Locate and identify every blood parasite.
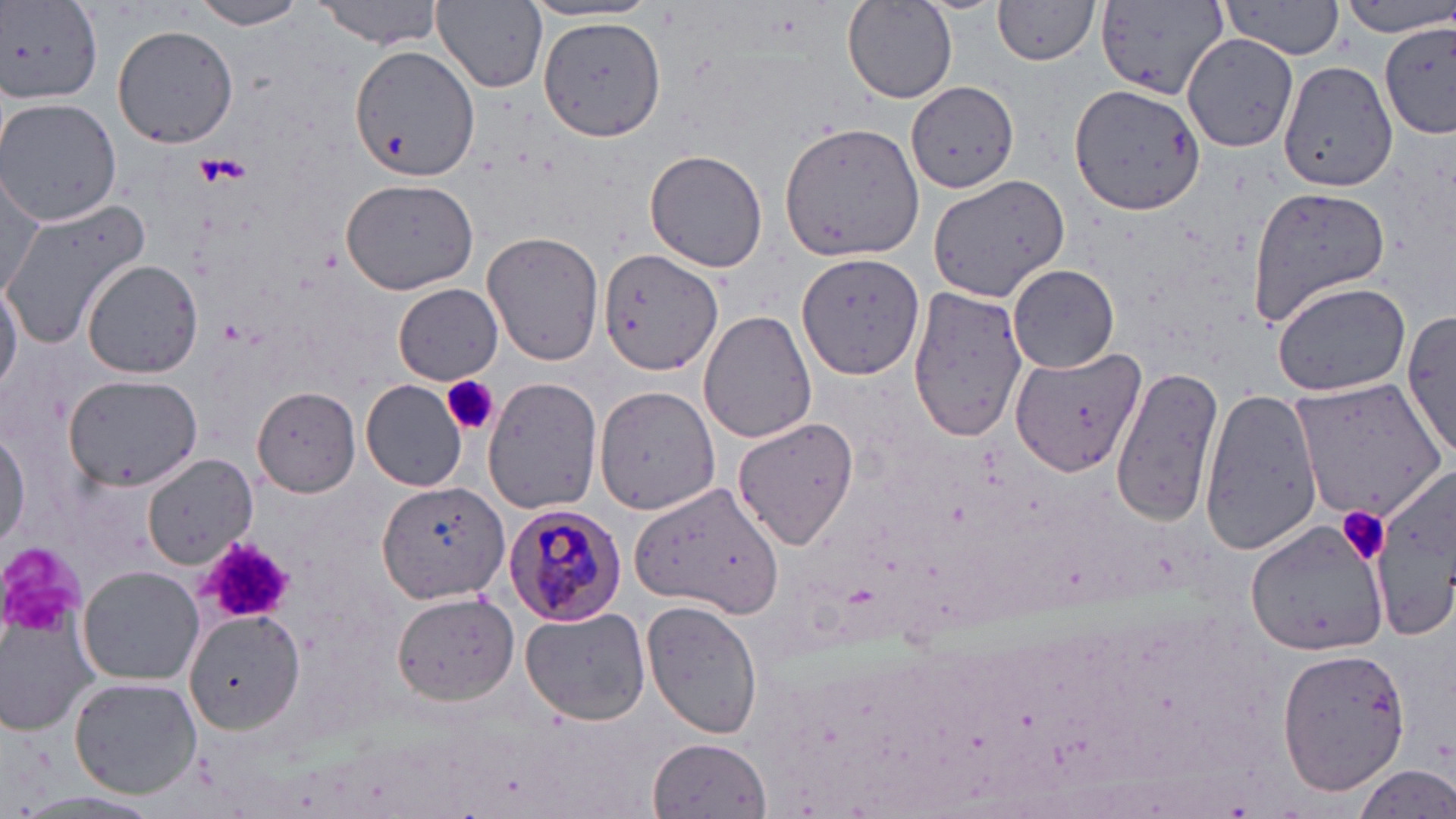
Approximate bounding boxes as (x1, y1, x2, y2) in pixels.
Plasmodium malariae-infected red blood cells: (502, 505, 627, 626).
No Plasmodium falciparum, Plasmodium ovale, Plasmodium vivax, Babesia divergens, or Trypanosoma brucei observed.

Summary:
  - Uninfected red blood cell locations: (314, 0, 447, 48), (433, 0, 548, 90), (1336, 0, 1456, 38), (189, 1, 308, 30), (992, 1, 1103, 65), (3, 2, 102, 103), (843, 2, 957, 102), (1218, 2, 1347, 57), (520, 3, 662, 26), (1091, 3, 1227, 104), (540, 15, 667, 141), (1378, 22, 1456, 137), (112, 25, 238, 150), (1183, 33, 1302, 153), (351, 45, 481, 182), (1279, 59, 1399, 192), (907, 81, 1019, 195), (1068, 81, 1208, 216), (0, 98, 122, 226), (779, 120, 925, 262), (644, 150, 769, 273), (2, 175, 48, 301), (927, 175, 1069, 299), (340, 176, 481, 295), (1246, 185, 1390, 319), (1, 200, 150, 347), (483, 232, 605, 368), (600, 246, 723, 376), (797, 253, 925, 380), (82, 260, 203, 380), (1009, 264, 1119, 373), (0, 273, 23, 398), (1270, 279, 1411, 397), (393, 283, 504, 384), (909, 287, 1026, 442), (698, 311, 816, 444), (1404, 312, 1456, 456), (1009, 335, 1139, 480), (1110, 361, 1227, 530), (64, 374, 200, 491), (483, 378, 602, 516), (1292, 378, 1450, 520), (362, 380, 468, 490), (594, 384, 723, 516), (252, 387, 361, 496), (1200, 387, 1321, 555), (733, 416, 859, 549), (0, 433, 26, 549), (142, 453, 258, 569), (1370, 473, 1455, 641), (628, 480, 785, 617), (378, 481, 511, 606), (1246, 521, 1387, 659), (77, 567, 204, 685), (392, 591, 518, 703), (641, 598, 763, 741), (1, 604, 100, 737), (518, 606, 650, 724), (186, 611, 303, 734), (1277, 645, 1411, 796), (68, 676, 201, 798), (647, 735, 772, 815), (1349, 765, 1456, 818), (4, 791, 170, 819)
  - Platelet locations: (442, 373, 499, 436), (1336, 506, 1391, 565), (198, 538, 299, 622), (0, 549, 82, 636)
  - Slide-level diagnosis: Plasmodium malariae
  - Image size: 1456×819 pixels
  - Preparation: thin blood smear
  - Modality: optical microscopy
  - Magnification: 1000x
  - Stain: May-Grünwald-Giemsa
  - Field of view: one of a larger specimen